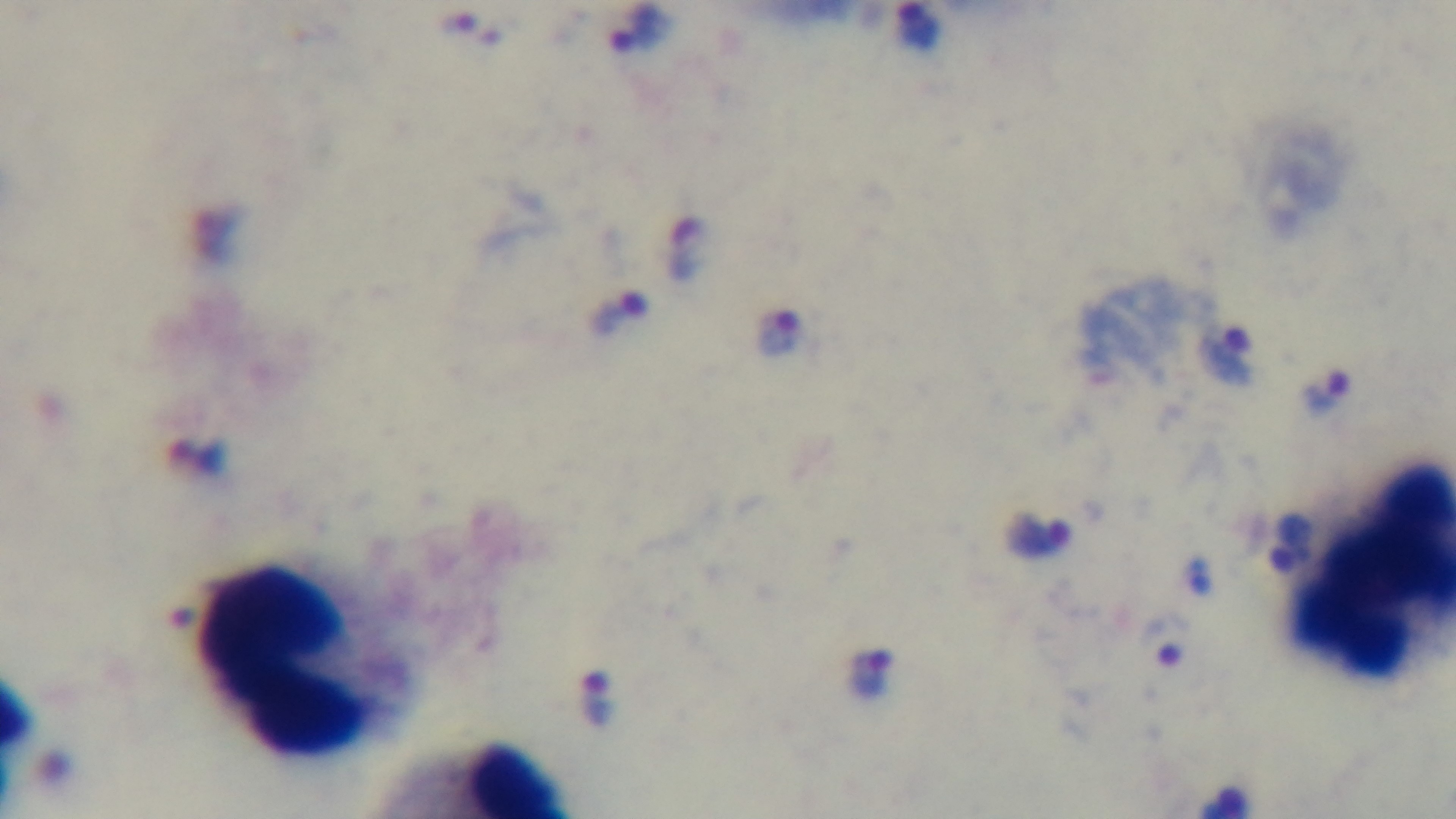 Mounted 4K digital camera. Oil-immersion objective, 100x. Malaria status: positive. Giemsa stain. Single field of view. Photomicrograph. Preparation: thick.